Identify the blood parasite species.
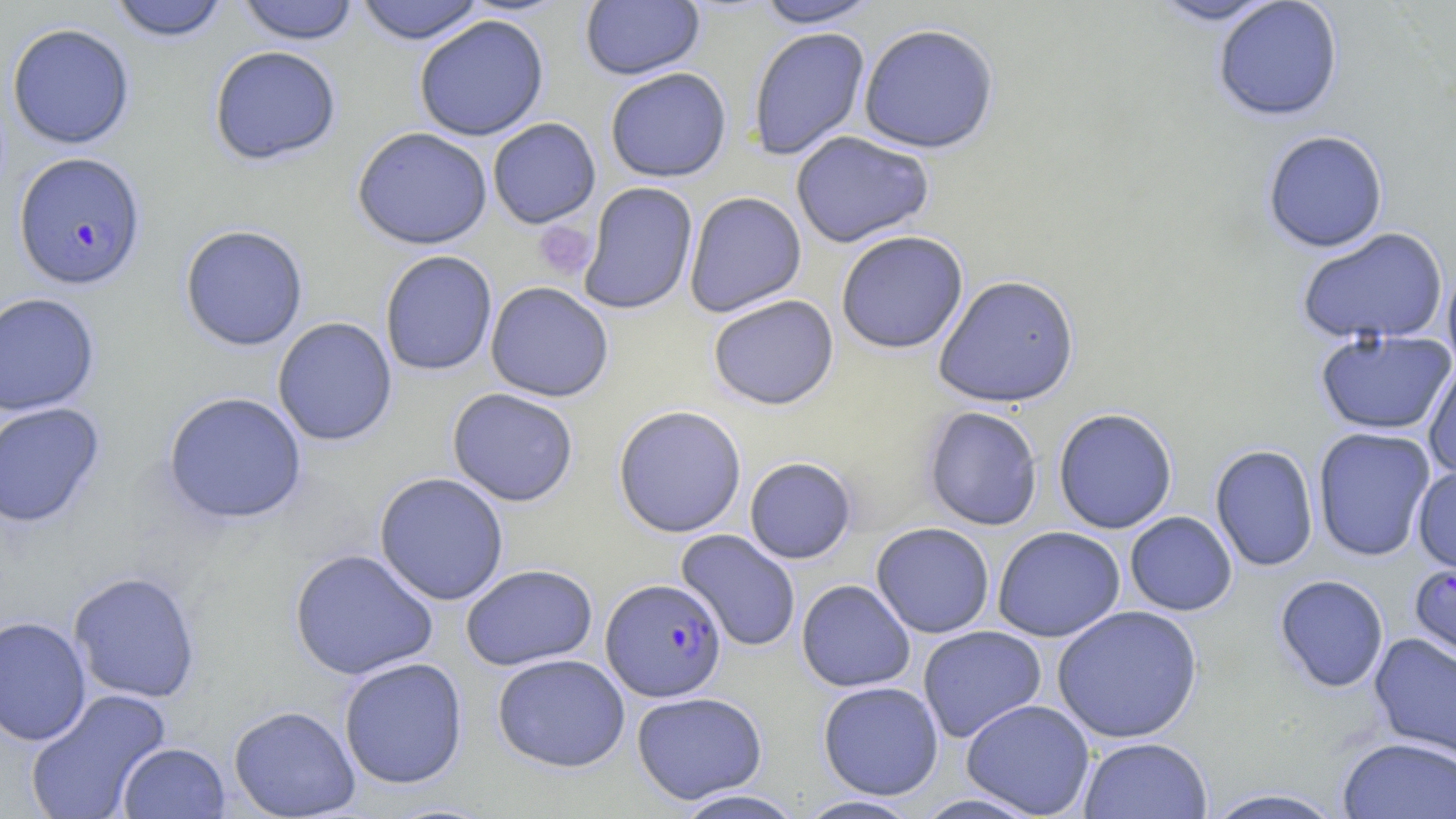
Plasmodium falciparum.

Summary:
  - Coordinate format: approximate bounding boxes as (x1, y1, x2, y2) in pixels
  - Uninfected red blood cell locations: (106, 0, 231, 43), (354, 0, 487, 45), (580, 0, 705, 80), (754, 0, 881, 29), (1146, 0, 1282, 26), (234, 1, 361, 45), (1212, 1, 1344, 122), (413, 14, 550, 141), (6, 22, 135, 150), (857, 23, 1000, 154), (747, 27, 871, 161), (208, 45, 342, 166), (604, 67, 732, 183), (487, 118, 601, 229), (352, 127, 493, 250), (1262, 129, 1389, 253), (790, 131, 935, 249), (579, 181, 698, 315), (684, 192, 807, 317), (178, 224, 309, 351), (1296, 227, 1449, 346), (835, 231, 969, 354), (379, 250, 498, 376), (1441, 260, 1456, 376), (932, 274, 1080, 408), (485, 282, 614, 402), (0, 292, 101, 416), (707, 294, 839, 410), (272, 317, 398, 447), (1315, 328, 1455, 436), (1423, 358, 1456, 480), (447, 388, 579, 506), (162, 391, 307, 526), (0, 402, 106, 529), (612, 405, 747, 538), (922, 405, 1043, 531), (1053, 407, 1178, 534), (1312, 427, 1436, 562), (1210, 444, 1318, 572), (744, 457, 857, 564), (1412, 464, 1456, 577), (373, 472, 510, 606), (1124, 511, 1238, 616), (871, 522, 995, 638), (992, 526, 1125, 642), (676, 529, 801, 652), (289, 548, 438, 681), (460, 564, 598, 671), (68, 571, 201, 703), (1274, 574, 1389, 693), (796, 579, 915, 692), (1051, 605, 1203, 743), (0, 616, 92, 746), (917, 625, 1046, 743), (1368, 632, 1456, 765), (492, 653, 630, 772), (338, 657, 468, 789), (817, 681, 944, 800), (24, 688, 172, 819), (631, 691, 768, 804), (961, 699, 1096, 818), (228, 705, 361, 818), (1077, 736, 1212, 819), (1337, 737, 1455, 819), (117, 742, 230, 818), (1201, 787, 1350, 819), (672, 789, 808, 818), (794, 795, 925, 818)
  - Plasmodium falciparum-infected red blood cell locations: (14, 152, 147, 291), (1409, 560, 1456, 669), (601, 578, 727, 702)
  - Platelet locations: (533, 220, 596, 281)
  - Modality: optical microscopy
  - Magnification: 1000x
  - Preparation: thin blood smear
  - Stain: May-Grünwald-Giemsa
  - Field of view: single
  - Image size: 1456×819 pixels